Give the position of every Plasmodium parasite.
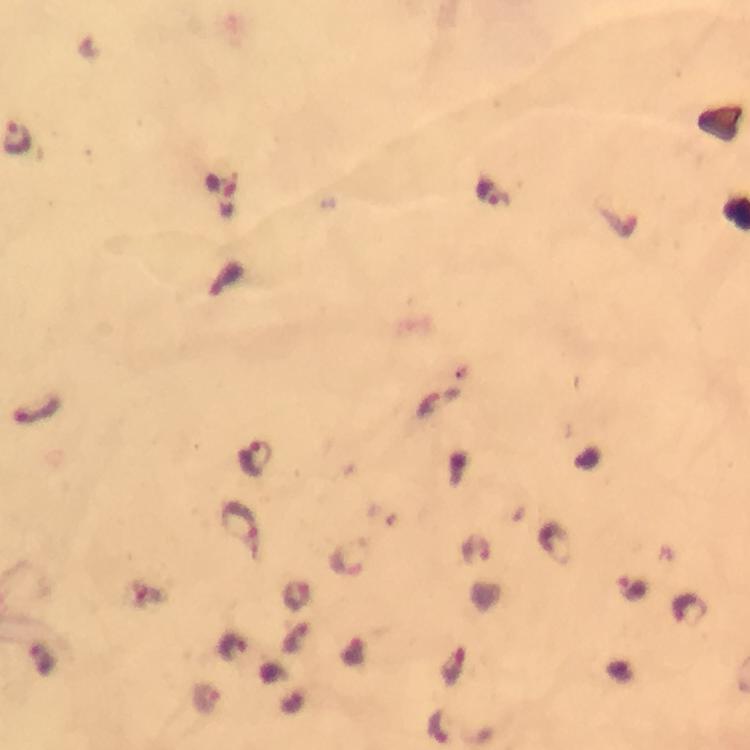

Approximate centers as {x, y} in pixels.
Plasmodium parasites: {17, 138}, {36, 410}, {253, 457}, {240, 520}, {346, 560}, {630, 588}, {295, 594}, {231, 644}, {205, 697}.

Summary:
  - Context: from a diagnostic examination for malaria
  - Capture: smartphone mounted on the microscope
  - Preparation: thick smear
  - Cropped from: one field of view
  - Immersion oil: applied
  - Image size: 750×750 pixels
  - Stain: Giemsa
  - Magnification: 100x